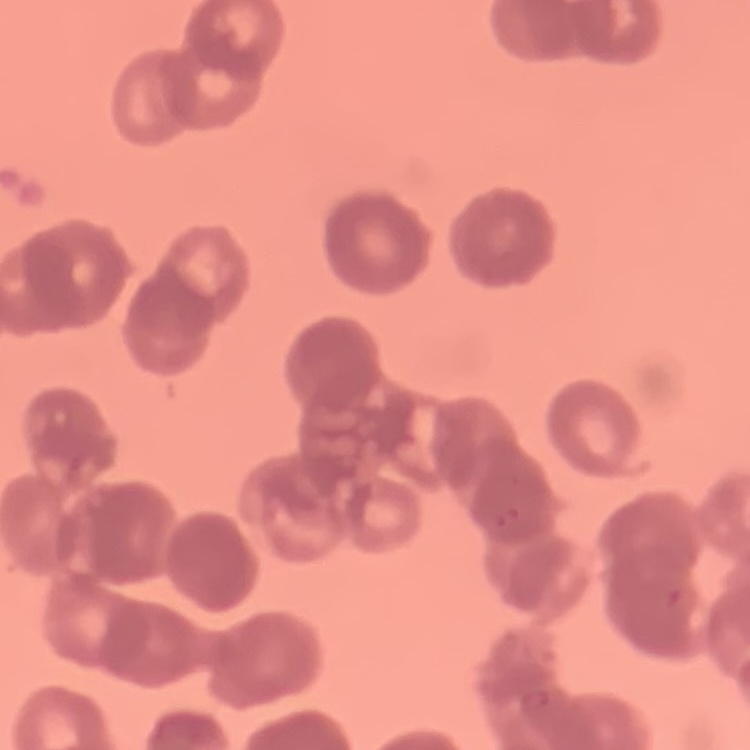

red blood cell morphology = rouleaux formation
image type = one tile cut from a larger photomicrograph
stain = Field's or Giemsa
preparation = thin blood film